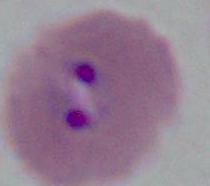
A Plasmodium parasite is shown. Photomicrograph. 400x or 1000x magnification.